Name the parasite shown.
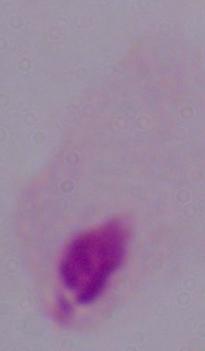

This is a trichomonad.

Summary:
  - Magnification: 1000x
  - Modality: photomicrograph